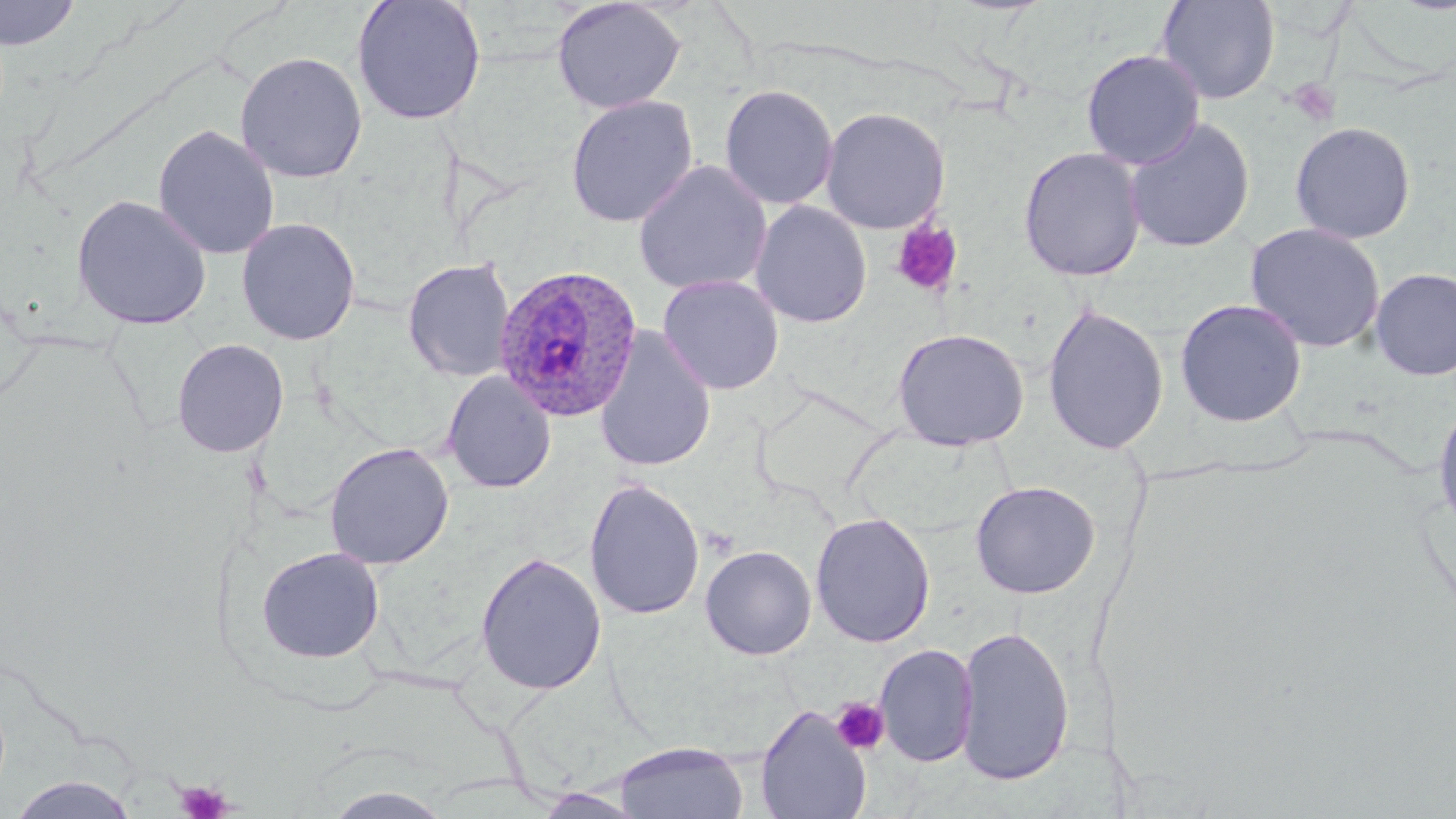

Summary:
  - Coordinate format: approximate bounding boxes as named x1/y1/x2/y2 corners in pixels
  - Platelet locations: (x1=1286, y1=79, x2=1340, y2=126), (x1=891, y1=219, x2=964, y2=298), (x1=830, y1=697, x2=890, y2=755), (x1=175, y1=780, x2=233, y2=819)
  - Uninfected red blood cell locations: (x1=0, y1=0, x2=80, y2=50), (x1=351, y1=0, x2=487, y2=126), (x1=551, y1=0, x2=686, y2=115), (x1=1156, y1=0, x2=1280, y2=105), (x1=1080, y1=49, x2=1205, y2=169), (x1=235, y1=51, x2=367, y2=184), (x1=719, y1=84, x2=839, y2=210), (x1=565, y1=94, x2=699, y2=228), (x1=820, y1=107, x2=950, y2=235), (x1=1123, y1=117, x2=1255, y2=254), (x1=1289, y1=121, x2=1417, y2=244), (x1=152, y1=124, x2=280, y2=260), (x1=1018, y1=146, x2=1147, y2=282), (x1=633, y1=159, x2=772, y2=296), (x1=72, y1=194, x2=212, y2=330), (x1=750, y1=200, x2=872, y2=328), (x1=236, y1=217, x2=361, y2=346), (x1=1244, y1=222, x2=1386, y2=353), (x1=402, y1=258, x2=515, y2=383), (x1=1370, y1=267, x2=1456, y2=381), (x1=658, y1=275, x2=784, y2=395), (x1=1174, y1=297, x2=1308, y2=427), (x1=1042, y1=303, x2=1169, y2=455), (x1=594, y1=326, x2=717, y2=473), (x1=892, y1=328, x2=1029, y2=450), (x1=171, y1=338, x2=289, y2=458), (x1=442, y1=371, x2=556, y2=494), (x1=1432, y1=398, x2=1456, y2=541), (x1=324, y1=442, x2=455, y2=570), (x1=583, y1=478, x2=705, y2=621), (x1=970, y1=480, x2=1101, y2=599), (x1=810, y1=512, x2=935, y2=648), (x1=700, y1=545, x2=817, y2=660), (x1=256, y1=547, x2=384, y2=664), (x1=474, y1=551, x2=607, y2=695), (x1=954, y1=624, x2=1075, y2=786), (x1=874, y1=644, x2=978, y2=767), (x1=755, y1=705, x2=872, y2=819), (x1=614, y1=742, x2=749, y2=819), (x1=6, y1=776, x2=143, y2=819), (x1=319, y1=785, x2=455, y2=819), (x1=531, y1=788, x2=651, y2=818)
  - Plasmodium ovale-infected red blood cell locations: (x1=493, y1=263, x2=644, y2=423)
  - Slide-level diagnosis: Plasmodium ovale
  - Magnification: 1000x
  - Modality: optical microscopy
  - Image size: 1456×819 pixels
  - Field of view: single
  - Stain: May-Grünwald-Giemsa
  - Preparation: thin blood film